State which parasite is depicted.
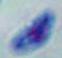

Toxoplasma gondii.

Summary:
  - Magnification: 1000x
  - Modality: micrograph